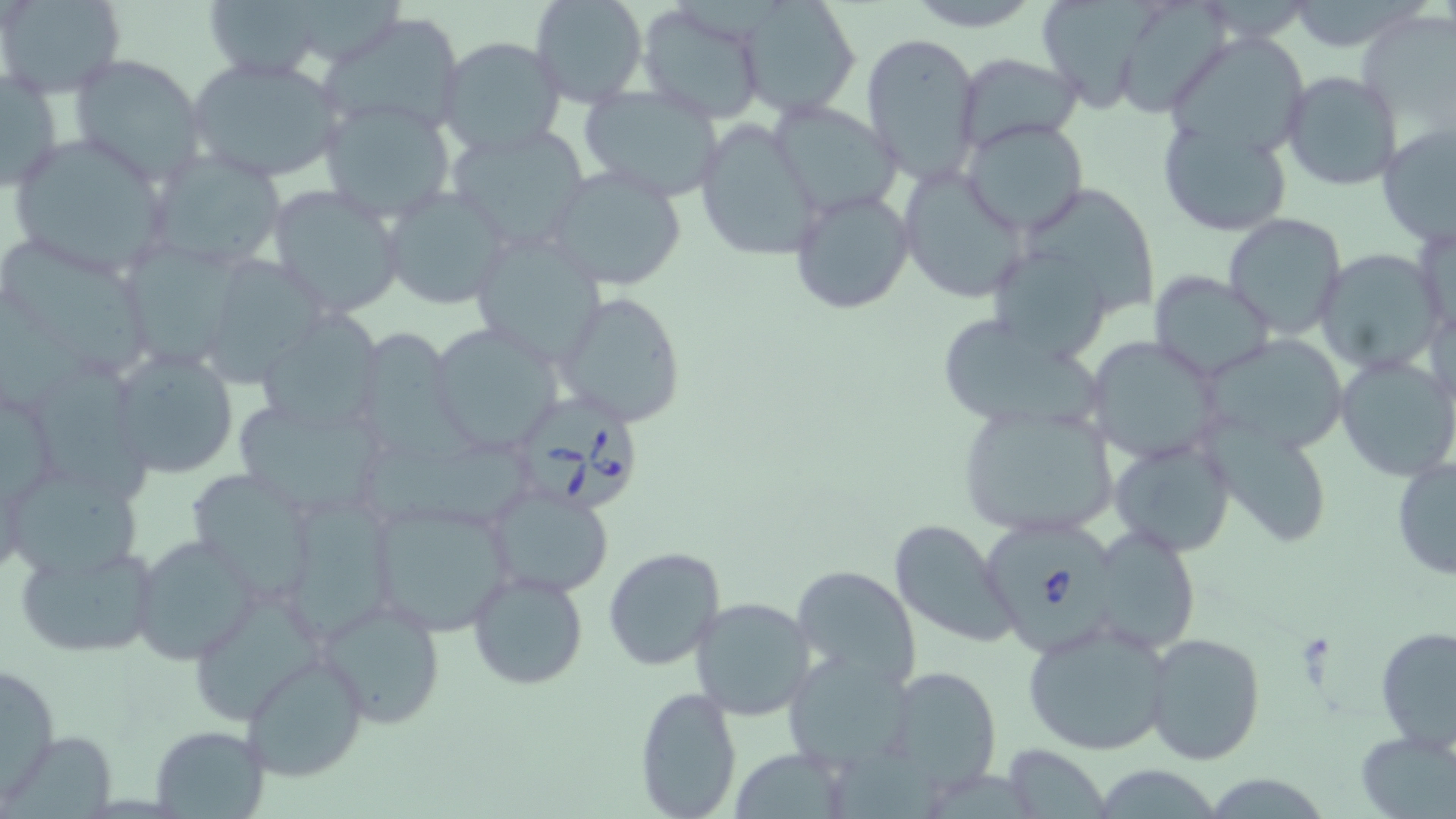 Approximate bounding boxes as [x1, y1, x2, y2] in pixels. Uninfected red blood cell locations: [1, 0, 125, 97], [201, 0, 328, 79], [529, 0, 649, 108], [736, 0, 863, 118], [905, 0, 1041, 30], [1043, 0, 1161, 113], [1286, 0, 1425, 53], [637, 1, 767, 122], [1123, 1, 1232, 122], [320, 12, 464, 136], [1360, 16, 1456, 123], [861, 32, 983, 183], [1178, 33, 1309, 158], [436, 36, 566, 156], [955, 52, 1085, 150], [68, 53, 208, 187], [186, 56, 346, 185], [1, 67, 63, 194], [1280, 71, 1402, 191], [575, 86, 725, 201], [320, 99, 456, 227], [766, 101, 901, 219], [695, 117, 824, 263], [1159, 117, 1294, 238], [960, 118, 1089, 236], [1377, 121, 1456, 246], [442, 123, 593, 251], [7, 133, 173, 277], [144, 149, 289, 273], [546, 164, 688, 291], [896, 167, 1031, 305], [265, 183, 407, 319], [381, 185, 512, 311], [789, 187, 914, 315], [1028, 187, 1156, 314], [1223, 212, 1346, 339], [467, 231, 608, 364], [0, 242, 147, 376], [120, 243, 250, 371], [1314, 250, 1445, 375], [210, 252, 327, 391], [994, 252, 1104, 359], [1149, 273, 1277, 379], [556, 291, 689, 426], [263, 314, 383, 431], [945, 318, 1096, 424], [430, 323, 567, 454], [361, 330, 473, 464], [1209, 333, 1345, 451], [1084, 336, 1224, 461], [106, 346, 241, 480], [1335, 354, 1456, 482], [34, 361, 148, 499], [956, 402, 1122, 540], [238, 403, 383, 513], [1203, 418, 1321, 549], [359, 435, 538, 529], [1110, 437, 1235, 555], [1390, 455, 1456, 583], [193, 473, 309, 602], [12, 477, 140, 578], [486, 484, 615, 598], [366, 498, 518, 637], [282, 500, 392, 642], [889, 518, 1019, 649], [1103, 531, 1196, 650], [129, 535, 261, 665], [14, 541, 162, 663], [603, 545, 726, 670], [790, 565, 921, 691], [468, 569, 588, 690], [314, 595, 448, 730], [689, 596, 815, 721], [1022, 620, 1173, 756], [1375, 625, 1456, 754], [1143, 631, 1266, 766], [243, 651, 371, 781], [780, 651, 918, 773], [1, 658, 61, 801], [884, 666, 1003, 788], [632, 686, 744, 819], [150, 727, 266, 814], [1352, 729, 1456, 818], [1003, 744, 1111, 819], [728, 747, 853, 819], [830, 751, 939, 819], [1103, 765, 1219, 819], [932, 773, 1035, 819], [1211, 777, 1322, 819]. Babesia divergens-infected red blood cell locations: [519, 390, 639, 514], [983, 516, 1133, 659]. Slide-level diagnosis: Babesia divergens. Image is 1456×819 pixels. May-Grünwald-Giemsa-stained preparation. Optical microscopy. One field of a larger specimen. Captured at 1000x magnification. Thin blood smear.